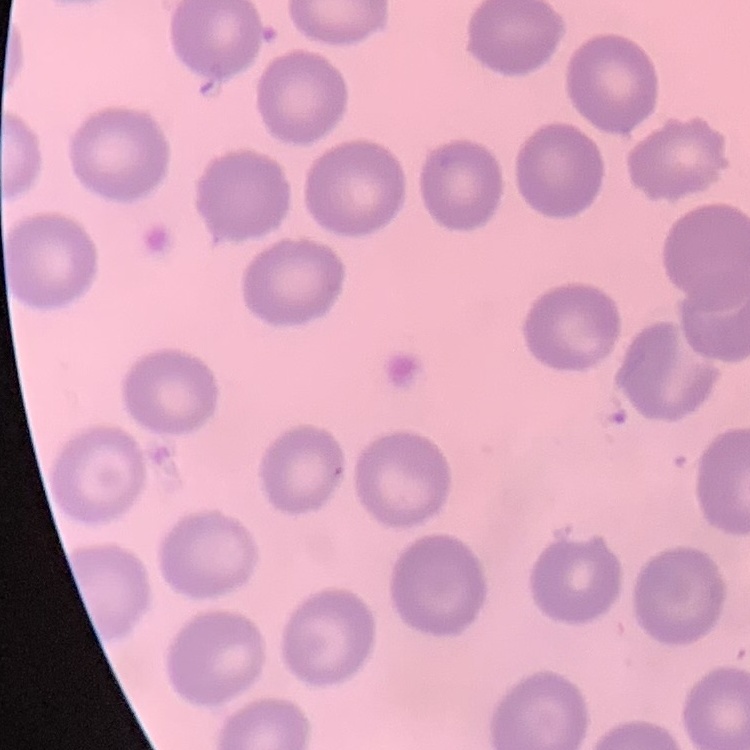
The red blood cells show no rouleaux formation. One tile cut from a larger photomicrograph. Thin peripheral smear. Field's or Giemsa stain.